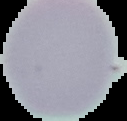
image_size: 127×121 pixels
image_type: cell region segmented out of the field of view; surrounding area masked to black
malaria_status: uninfected
preparation: thin blood smear